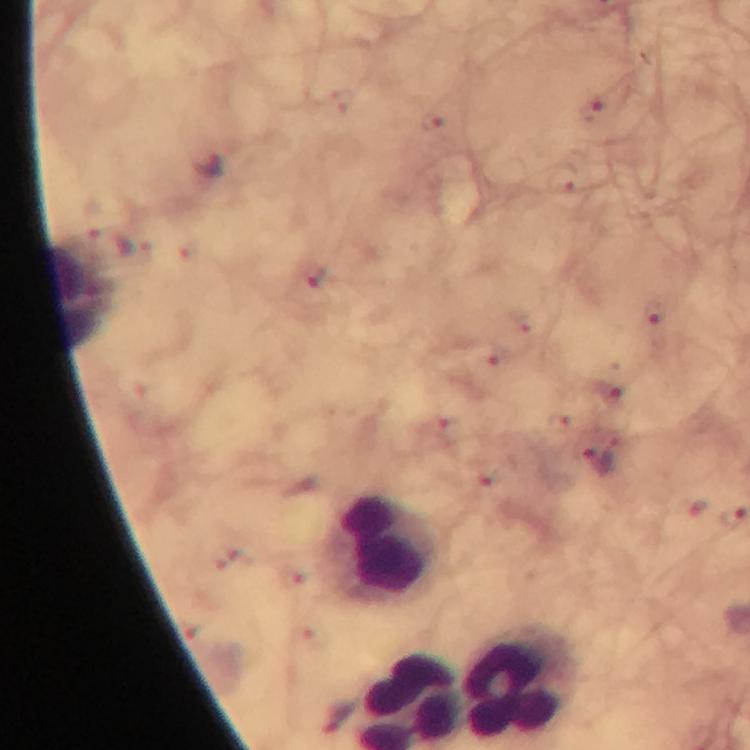

Approximate centers as [x, y] in pixels.
Summary:
  - Leukocyte locations: [79, 297], [385, 545], [520, 686]
  - Malaria parasite locations: [209, 167], [653, 317], [598, 464]
  - Image size: 750×750 pixels
  - Cropped from: a single field of view
  - Stain: Giemsa
  - Capture: smartphone camera through the microscope
  - Preparation: thick blood film
  - Context: from a diagnostic examination for malaria
  - Magnification: 100x
  - Immersion oil: used